Look for Plasmodium parasites.
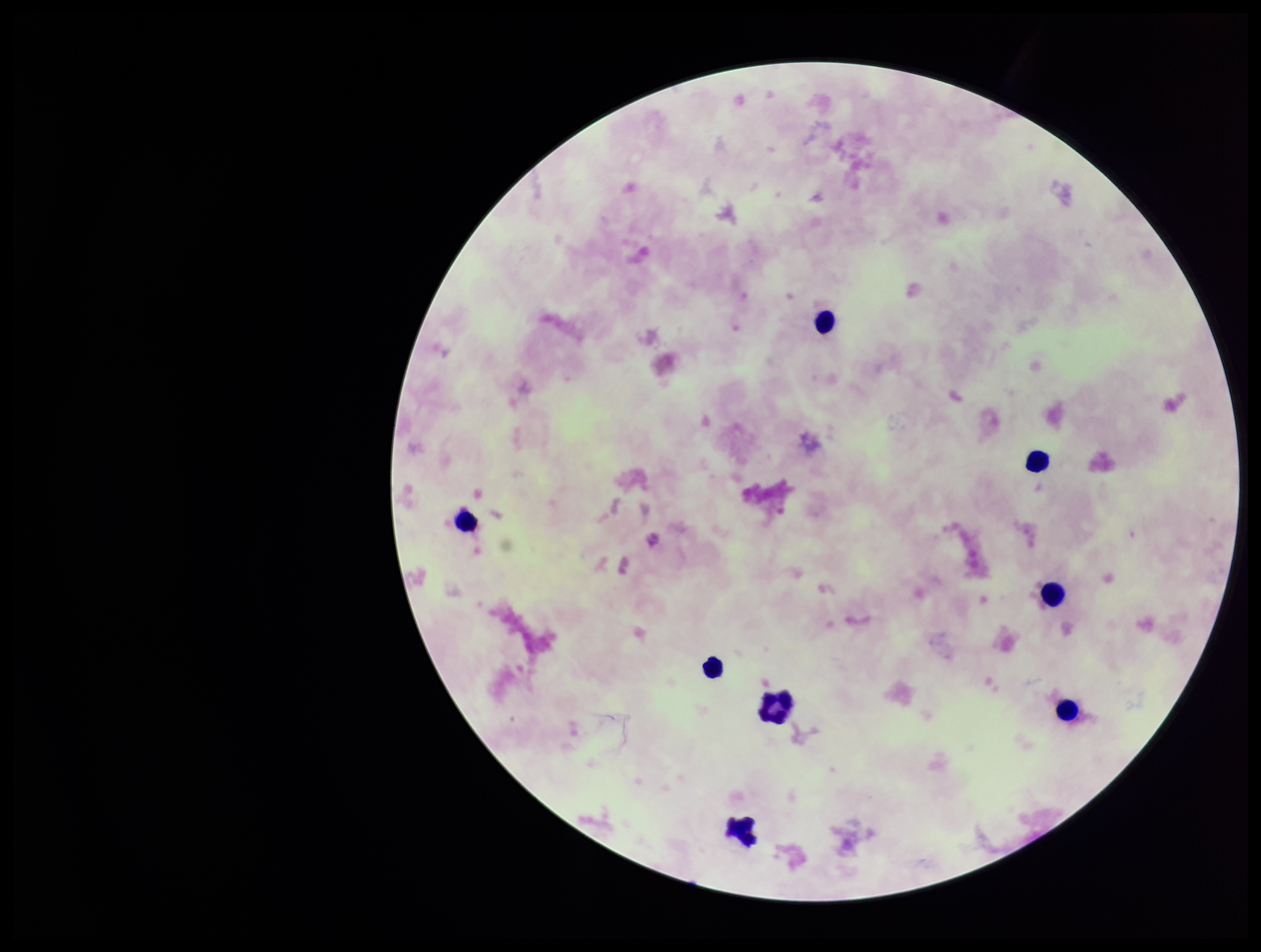
None identified.

image size = 1261×952 pixels
preparation = thick smear
leukocyte count = 8
capture = smartphone photograph through the microscope eyepiece
field of view = one from this slide
stain = Giemsa
patient malaria status = negative
parasite count = 0